Outline every malaria parasite.
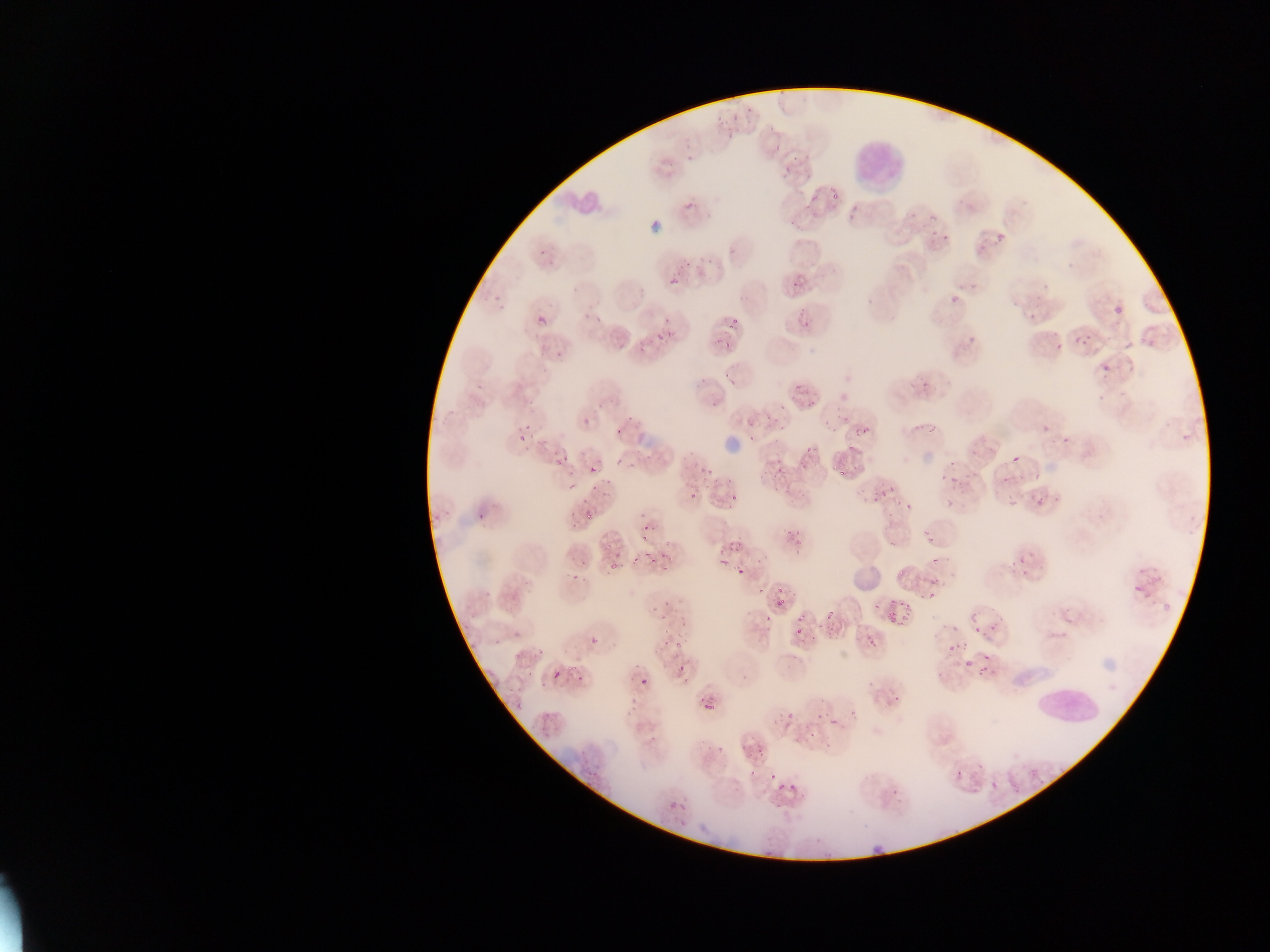

Approximate bounding boxes as left top right bottom in pixels.
Malaria parasites: 709 109 741 137; 775 132 808 176; 685 180 721 213; 792 186 815 208; 844 210 854 221; 924 220 958 249; 651 221 660 231; 997 233 1005 240; 537 241 558 261; 700 254 711 264; 665 262 683 291; 788 278 803 293; 487 288 503 310; 937 291 955 311; 532 300 558 328; 794 302 814 335; 1115 306 1123 316; 591 317 601 334; 963 321 979 348; 650 323 673 350; 706 325 742 348; 609 328 635 352; 1070 330 1098 347; 535 340 552 351; 1040 344 1054 361; 1095 350 1124 383; 553 358 566 368; 792 380 824 406; 911 383 929 404; 699 393 716 410; 908 414 942 439; 577 415 593 425; 841 416 849 425; 855 417 871 453; 517 419 530 447; 613 424 631 444; 1041 425 1049 434; 745 427 766 446; 1061 437 1069 445; 551 447 557 460; 562 448 581 474; 798 450 827 466; 619 451 630 457; 657 451 673 468; 1012 455 1020 463; 680 458 708 481; 837 464 857 481; 935 466 968 493; 776 467 785 477; 583 471 614 513; 710 484 738 498; 994 484 1014 503; 886 489 900 506; 681 491 707 509; 859 491 874 508; 1023 493 1044 508; 472 499 495 522; 777 506 829 545; 922 506 943 538; 573 512 587 529; 715 530 750 561; 598 542 621 561; 1007 553 1045 580; 644 555 667 572; 744 560 783 596; 563 562 588 585; 725 562 742 576; 929 563 949 584; 1143 582 1163 616; 1127 585 1140 604; 655 589 673 606; 900 595 917 618; 766 601 787 619; 1058 605 1098 638; 825 612 833 619; 888 613 896 621; 972 616 1004 637; 790 621 821 646; 858 625 888 653; 656 629 679 646; 506 631 519 639; 942 634 962 665; 589 637 598 646; 514 649 531 662; 966 656 995 678; 668 661 681 674; 549 665 563 682; 637 679 647 689; 880 691 894 709; 809 698 853 730; 706 703 714 712; 771 709 797 731; 631 711 649 736; 808 719 834 760; 741 721 775 760; 716 746 725 754; 725 764 746 780; 760 772 783 792; 943 776 971 799; 785 787 811 815; 891 787 899 795; 990 787 1011 809; 668 797 689 816; 864 845 891 867 | approximate x y pixel centers of objects too small to bound: 644 526.

Leukocyte locations: 835 127 903 191; 560 192 612 222; 1027 679 1096 742. Thin blood smear. Photographed through a microscope with a mobile-phone camera. Single field of view. Image is 1270×952 pixels. Collected in Ghana.